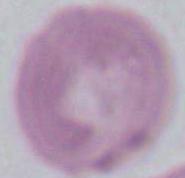
identification: erythrocyte
modality: micrograph
magnification: 1000x